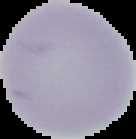
image size = 136×139 pixels
preparation = thin blood film
image type = segmented cell region on a black background
result = negative for malaria parasites